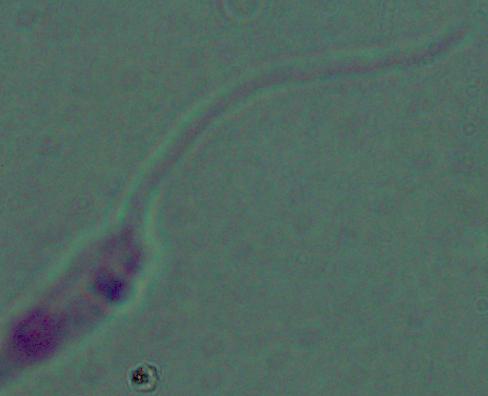

Micrograph. A Leishmania parasite is seen. 1000x magnification.